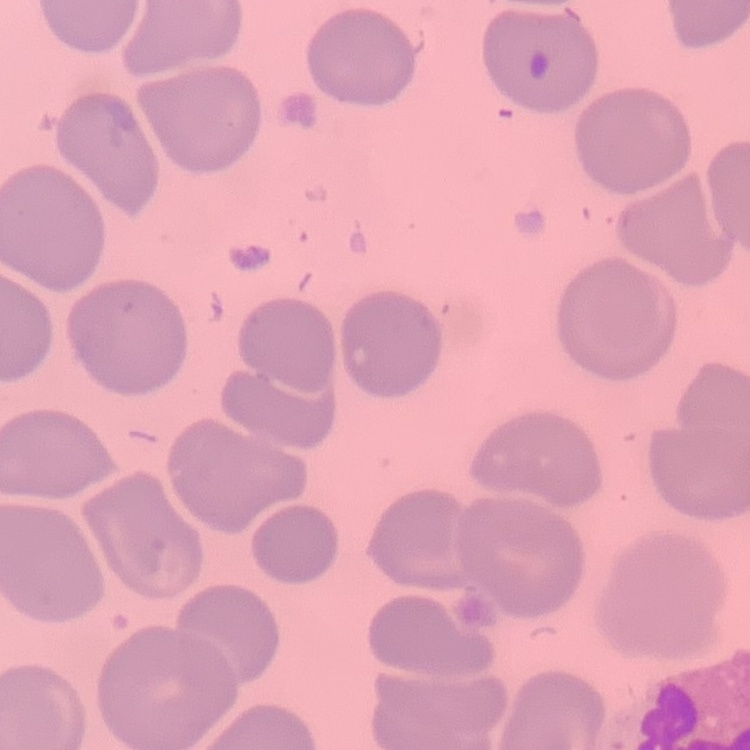

Summary:
  - Red blood cell morphology: no rouleaux formation
  - Image type: one tile cut from a larger photomicrograph
  - Preparation: thin blood smear
  - Stain: Field's or Giemsa